Assess this cell for malaria.
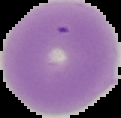

It is uninfected.

preparation = thin blood smear
image size = 121×118 pixels
image type = cell region segmented out of the field of view; surrounding area masked to black